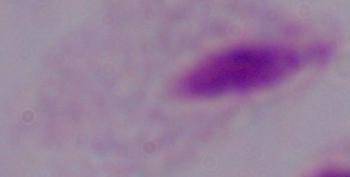

Summary:
  - Magnification: 1000x
  - Modality: micrograph
  - Identification: trichomonad